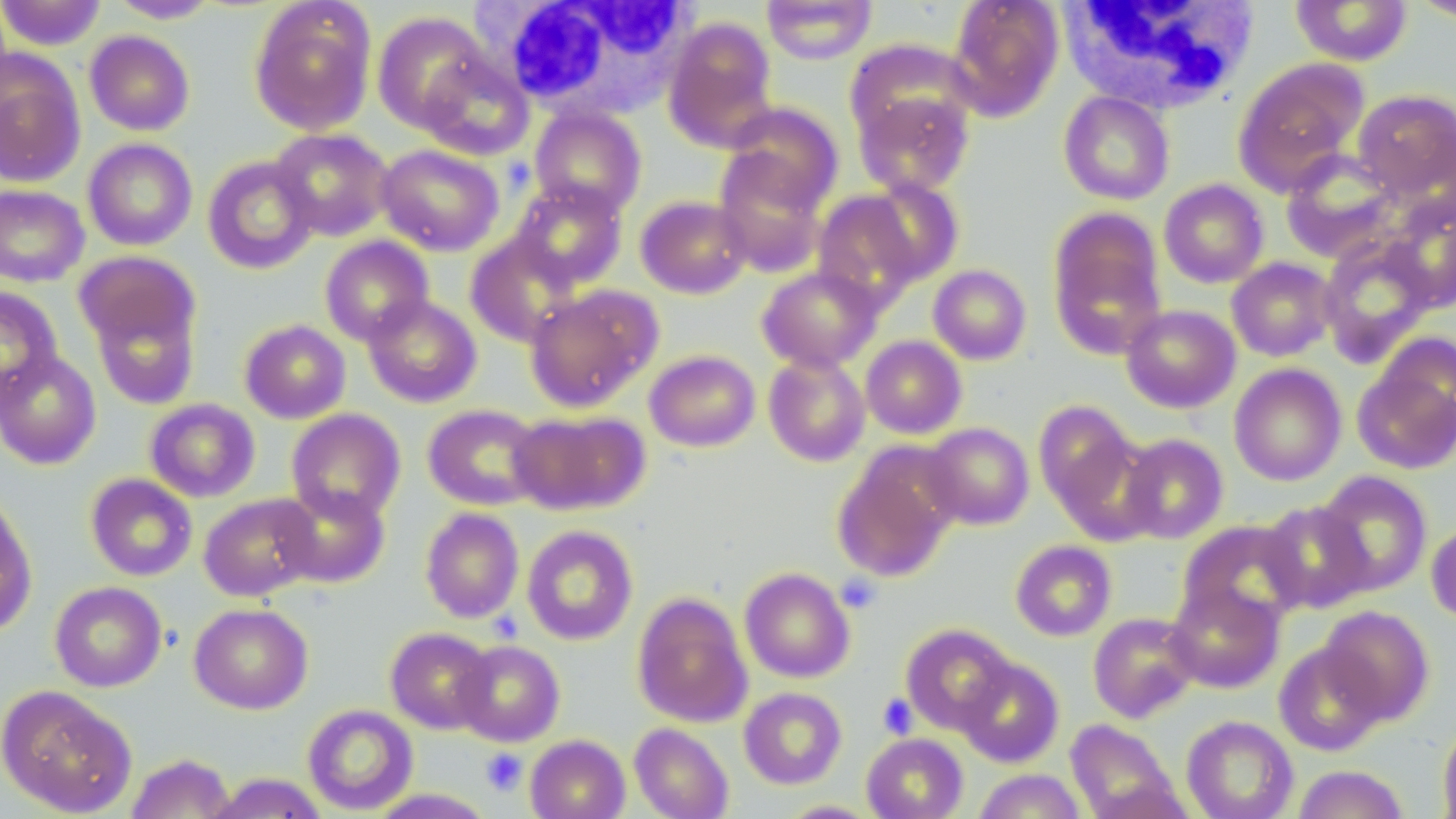

Summary:
  - Coordinate format: approximate bounding boxes as [x1, y1, x2, y2] in pixels
  - Uninfected red blood cell locations: [0, 0, 106, 50], [761, 0, 878, 65], [946, 0, 1066, 122], [1290, 0, 1413, 66], [107, 1, 222, 23], [1409, 1, 1456, 23], [248, 2, 377, 135], [371, 11, 491, 133], [662, 16, 778, 151], [84, 30, 195, 136], [843, 38, 976, 147], [416, 51, 534, 161], [0, 53, 86, 187], [1231, 58, 1368, 196], [855, 87, 975, 197], [1352, 88, 1456, 203], [1058, 91, 1175, 205], [721, 102, 843, 214], [529, 106, 647, 218], [269, 127, 395, 241], [83, 138, 197, 251], [376, 143, 504, 256], [712, 149, 830, 276], [1280, 149, 1399, 261], [202, 155, 319, 274], [858, 177, 964, 286], [1158, 179, 1269, 288], [510, 181, 628, 290], [0, 184, 90, 287], [812, 189, 926, 312], [635, 194, 751, 299], [1380, 199, 1456, 312], [1046, 207, 1167, 359], [464, 232, 581, 347], [319, 235, 434, 345], [1317, 236, 1435, 364], [74, 251, 200, 353], [1226, 257, 1338, 361], [928, 264, 1032, 365], [756, 265, 882, 372], [524, 285, 661, 412], [0, 286, 63, 408], [89, 295, 201, 410], [363, 295, 482, 408], [1120, 304, 1241, 413], [239, 319, 351, 424], [860, 335, 967, 439], [0, 349, 102, 470], [644, 349, 761, 452], [1352, 349, 1456, 476], [763, 352, 871, 467], [1229, 363, 1347, 486], [144, 398, 261, 502], [1033, 400, 1143, 526], [423, 403, 545, 511], [286, 408, 405, 523], [507, 410, 649, 515], [923, 422, 1035, 530], [1118, 433, 1229, 544], [831, 444, 960, 584], [1314, 470, 1433, 596], [85, 473, 198, 581], [276, 484, 390, 588], [199, 493, 321, 601], [0, 495, 37, 637], [1258, 500, 1373, 613], [420, 507, 524, 623], [1176, 519, 1307, 627], [1426, 520, 1456, 626], [521, 524, 638, 645], [1010, 540, 1117, 641], [739, 567, 855, 683], [49, 581, 167, 692], [1165, 582, 1285, 694], [631, 591, 753, 728], [189, 602, 313, 714], [1318, 605, 1435, 726], [1088, 612, 1201, 723], [900, 623, 1015, 734], [386, 627, 494, 733], [452, 640, 565, 747], [1273, 641, 1387, 756], [956, 657, 1064, 767], [0, 685, 137, 817], [738, 687, 847, 789], [302, 704, 418, 815], [1181, 715, 1298, 819], [1065, 719, 1182, 819], [1437, 722, 1456, 819], [629, 723, 734, 819], [861, 733, 968, 819], [525, 734, 630, 819], [126, 753, 235, 818], [1292, 764, 1410, 819], [972, 769, 1087, 819], [205, 772, 329, 818], [366, 788, 497, 818], [777, 800, 882, 818]
  - Platelet locations: [835, 573, 881, 613], [878, 693, 918, 739], [480, 748, 527, 796]
  - White blood cell locations: [497, 1, 694, 119], [1059, 1, 1262, 115]
  - Slide-level diagnosis: negative for blood parasites
  - Image size: 1456×819 pixels
  - Preparation: thin blood smear
  - Stain: May-Grünwald-Giemsa
  - Field of view: one of a larger specimen
  - Magnification: 1000x
  - Modality: light microscopy